Locate and identify every blood parasite.
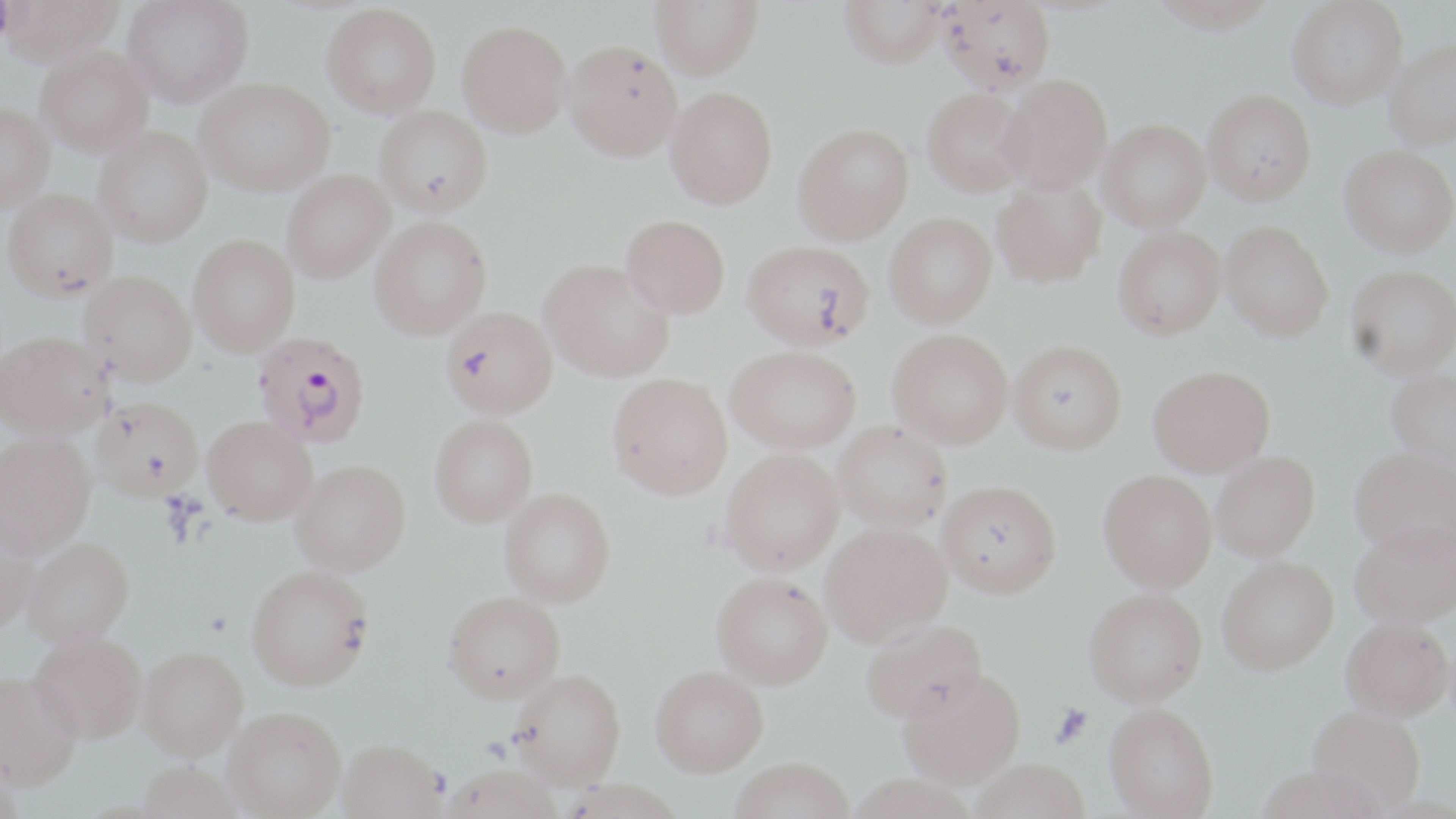
Approximate bounding boxes as (x1,y1)-(x2,y2) corner pairs in pixels.
Plasmodium falciparum-infected red blood cells: (253,331)-(370,447).
No Plasmodium ovale, Plasmodium malariae, Plasmodium vivax, Babesia divergens, or Trypanosoma brucei observed.

Uninfected red blood cell locations: (0,0)-(125,66), (122,0)-(253,107), (650,0)-(763,79), (839,0)-(949,68), (939,0)-(1055,95), (1146,0)-(1280,33), (1287,0)-(1408,108), (322,4)-(441,117), (457,20)-(572,137), (1384,38)-(1456,149), (564,40)-(682,161), (36,46)-(153,157), (997,74)-(1112,195), (196,77)-(334,196), (665,86)-(778,209), (922,88)-(1030,196), (1203,88)-(1316,205), (0,102)-(54,211), (374,106)-(493,216), (1097,119)-(1211,232), (793,123)-(913,244), (93,127)-(212,247), (1340,145)-(1456,256), (282,170)-(394,283), (992,176)-(1106,288), (3,188)-(117,300), (884,213)-(997,328), (620,215)-(730,319), (370,216)-(491,339), (1220,220)-(1334,341), (1113,226)-(1226,340), (188,235)-(300,356), (742,240)-(874,351), (538,259)-(673,381), (1346,265)-(1456,378), (80,270)-(196,385), (441,306)-(557,419), (888,328)-(1013,448), (0,329)-(113,439), (1009,340)-(1127,454), (726,345)-(860,454), (1148,365)-(1275,476), (1387,369)-(1456,470), (607,373)-(732,499), (91,395)-(203,500), (203,415)-(317,525), (430,415)-(538,527), (833,421)-(952,531), (0,432)-(95,557), (1349,446)-(1456,559), (720,448)-(844,575), (1211,451)-(1320,561), (291,460)-(410,575), (1098,470)-(1217,592), (938,479)-(1061,597), (499,488)-(616,607), (0,513)-(39,632), (820,520)-(951,646), (1349,520)-(1456,628), (24,537)-(134,646), (1217,556)-(1339,674), (247,565)-(374,690), (711,571)-(833,689), (1084,588)-(1207,706), (443,591)-(565,703), (860,618)-(986,724), (1341,618)-(1454,722), (29,630)-(147,744), (138,646)-(248,759), (651,665)-(768,775), (898,666)-(1025,788), (509,668)-(626,788), (0,670)-(82,790), (1104,703)-(1219,818), (1307,705)-(1425,814), (224,706)-(345,818), (338,739)-(447,819), (729,758)-(854,819), (969,759)-(1091,819), (138,761)-(242,819), (440,763)-(563,819). Platelet locations: (0,2)-(15,42), (1051,704)-(1092,747). Slide-level diagnosis: Plasmodium falciparum. One field of a larger specimen. Light microscopy. Thin blood film. 1000x magnification. Image is 1456×819 pixels. May-Grünwald-Giemsa stain.